Comment on the morphology of the red blood cells.
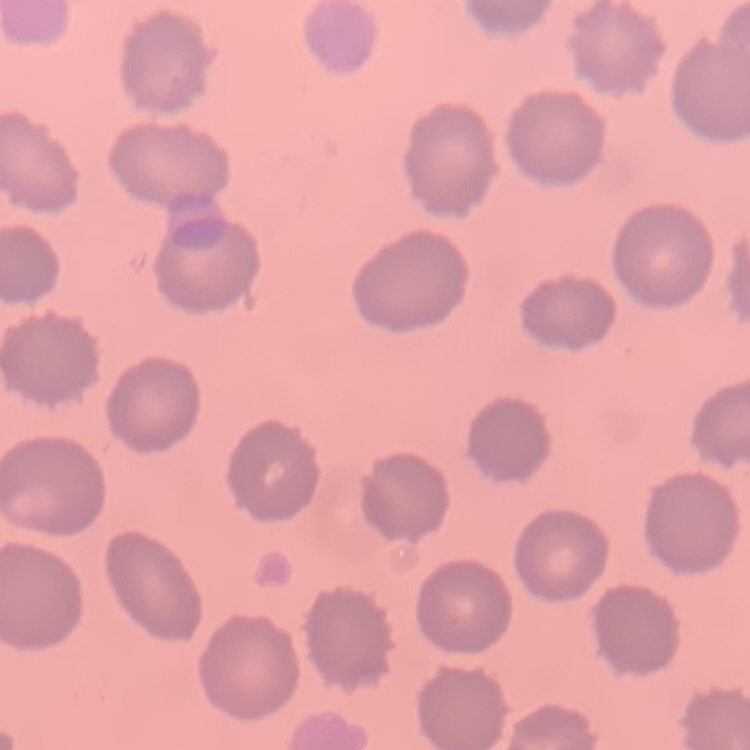

No rouleaux formation.

Summary:
  - Image type: square crop of a larger photomicrograph
  - Stain: Field's or Giemsa
  - Preparation: thin peripheral smear